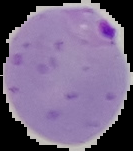

Summary:
  - Preparation: thin blood film
  - Result: malaria parasites detected
  - Image type: segmented cell region with the area outside set to black
  - Image size: 133×151 pixels